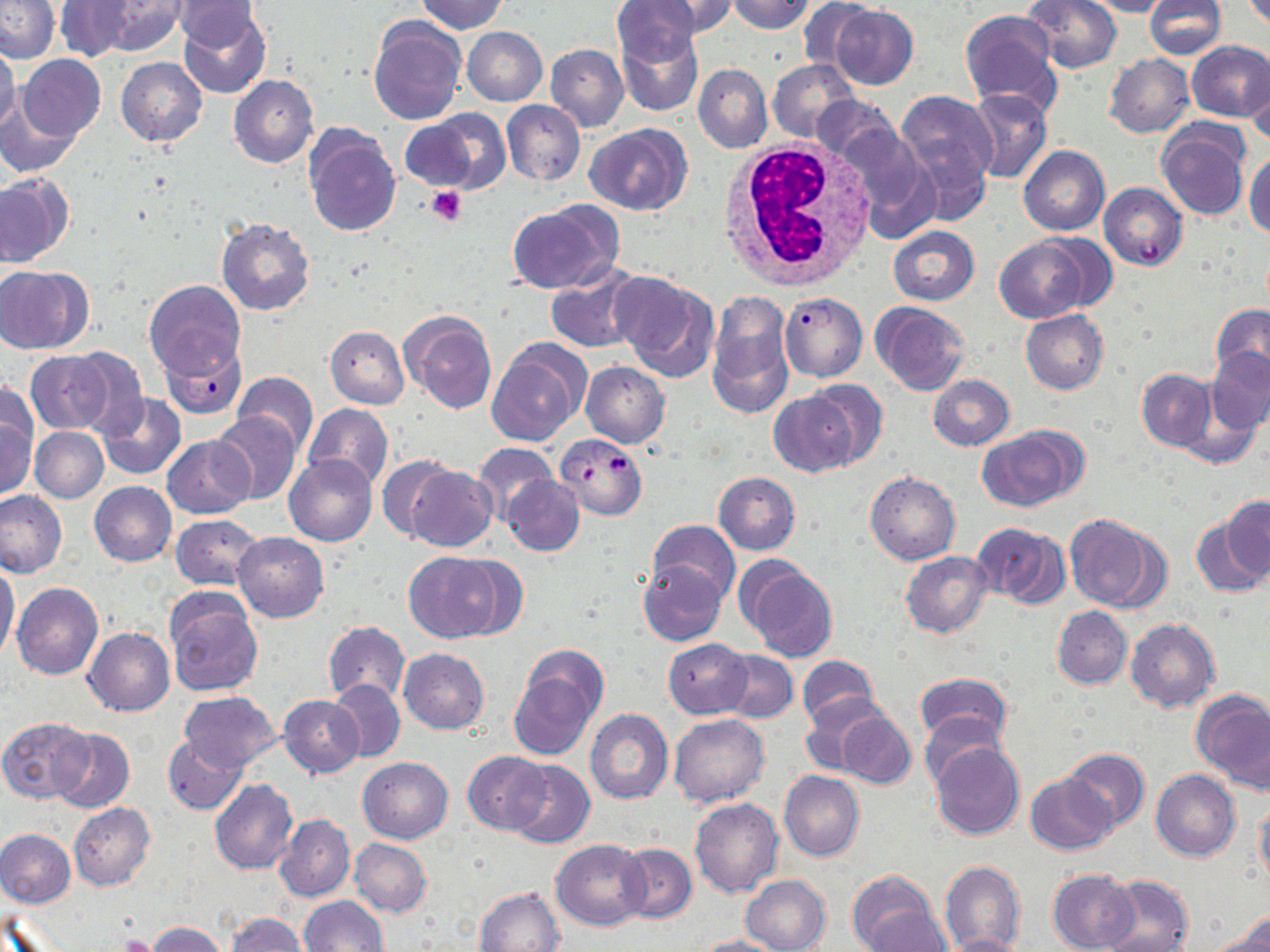
Approximate bounding boxes as named x1/y1/x2/y2 corners in pixels. Plasmodium falciparum-infected red blood cell locations: (x1=1098, y1=183, x2=1188, y2=270), (x1=778, y1=291, x2=867, y2=383), (x1=161, y1=339, x2=246, y2=419), (x1=556, y1=434, x2=648, y2=519). White blood cell locations: (x1=716, y1=139, x2=877, y2=291). Uninfected red blood cell locations: (x1=1, y1=0, x2=60, y2=63), (x1=415, y1=0, x2=508, y2=34), (x1=611, y1=0, x2=707, y2=68), (x1=639, y1=0, x2=743, y2=38), (x1=726, y1=0, x2=817, y2=34), (x1=1024, y1=0, x2=1122, y2=73), (x1=1086, y1=0, x2=1170, y2=18), (x1=1144, y1=0, x2=1227, y2=60), (x1=96, y1=1, x2=187, y2=57), (x1=171, y1=1, x2=265, y2=49), (x1=799, y1=1, x2=873, y2=74), (x1=54, y1=2, x2=133, y2=63), (x1=177, y1=5, x2=271, y2=99), (x1=830, y1=5, x2=918, y2=88), (x1=959, y1=10, x2=1061, y2=112), (x1=369, y1=17, x2=465, y2=125), (x1=616, y1=24, x2=705, y2=118), (x1=463, y1=27, x2=547, y2=106), (x1=1185, y1=40, x2=1270, y2=122), (x1=0, y1=41, x2=20, y2=134), (x1=546, y1=44, x2=629, y2=133), (x1=1104, y1=54, x2=1195, y2=139), (x1=17, y1=55, x2=105, y2=141), (x1=116, y1=57, x2=207, y2=147), (x1=768, y1=59, x2=859, y2=143), (x1=693, y1=64, x2=773, y2=153), (x1=1246, y1=68, x2=1269, y2=145), (x1=228, y1=75, x2=320, y2=169), (x1=965, y1=89, x2=1052, y2=183), (x1=0, y1=90, x2=79, y2=179), (x1=893, y1=93, x2=994, y2=209), (x1=811, y1=94, x2=901, y2=166), (x1=501, y1=99, x2=586, y2=186), (x1=406, y1=111, x2=502, y2=193), (x1=1156, y1=122, x2=1249, y2=221), (x1=586, y1=124, x2=692, y2=216), (x1=304, y1=125, x2=401, y2=237), (x1=832, y1=126, x2=940, y2=244), (x1=1018, y1=146, x2=1109, y2=235), (x1=1245, y1=150, x2=1270, y2=239), (x1=0, y1=173, x2=72, y2=268), (x1=507, y1=203, x2=620, y2=295), (x1=217, y1=218, x2=314, y2=314), (x1=887, y1=225, x2=978, y2=306), (x1=1031, y1=233, x2=1117, y2=312), (x1=994, y1=237, x2=1091, y2=323), (x1=546, y1=261, x2=645, y2=353), (x1=0, y1=265, x2=91, y2=354), (x1=613, y1=274, x2=721, y2=383), (x1=144, y1=279, x2=245, y2=384), (x1=707, y1=291, x2=794, y2=417), (x1=871, y1=302, x2=969, y2=394), (x1=1212, y1=305, x2=1270, y2=386), (x1=400, y1=308, x2=497, y2=415), (x1=1020, y1=310, x2=1109, y2=394), (x1=326, y1=326, x2=409, y2=409), (x1=488, y1=339, x2=591, y2=447), (x1=63, y1=346, x2=149, y2=438), (x1=1206, y1=348, x2=1270, y2=434), (x1=25, y1=351, x2=111, y2=434), (x1=580, y1=361, x2=669, y2=448), (x1=1136, y1=368, x2=1215, y2=451), (x1=232, y1=373, x2=318, y2=455), (x1=928, y1=374, x2=1015, y2=450), (x1=803, y1=379, x2=888, y2=469), (x1=0, y1=380, x2=38, y2=465), (x1=768, y1=391, x2=859, y2=477), (x1=96, y1=392, x2=187, y2=480), (x1=304, y1=404, x2=392, y2=491), (x1=212, y1=412, x2=300, y2=506), (x1=0, y1=419, x2=36, y2=501), (x1=977, y1=426, x2=1084, y2=512), (x1=30, y1=427, x2=109, y2=503), (x1=163, y1=435, x2=254, y2=518), (x1=473, y1=443, x2=559, y2=524), (x1=285, y1=455, x2=376, y2=547), (x1=376, y1=456, x2=458, y2=542), (x1=405, y1=465, x2=497, y2=552), (x1=865, y1=471, x2=960, y2=565), (x1=713, y1=472, x2=801, y2=554), (x1=503, y1=476, x2=584, y2=556), (x1=89, y1=481, x2=177, y2=566), (x1=0, y1=490, x2=69, y2=579), (x1=1224, y1=496, x2=1270, y2=583), (x1=1192, y1=510, x2=1269, y2=598), (x1=172, y1=515, x2=261, y2=590), (x1=1066, y1=516, x2=1162, y2=612), (x1=645, y1=519, x2=740, y2=604), (x1=972, y1=523, x2=1070, y2=609), (x1=234, y1=532, x2=329, y2=622), (x1=403, y1=551, x2=510, y2=642), (x1=900, y1=551, x2=993, y2=639), (x1=638, y1=559, x2=726, y2=646), (x1=739, y1=559, x2=840, y2=663), (x1=0, y1=563, x2=20, y2=661), (x1=12, y1=582, x2=103, y2=680), (x1=163, y1=590, x2=263, y2=698), (x1=1052, y1=606, x2=1132, y2=690), (x1=1125, y1=618, x2=1220, y2=712), (x1=323, y1=622, x2=409, y2=704), (x1=84, y1=628, x2=175, y2=716), (x1=664, y1=638, x2=753, y2=718), (x1=398, y1=648, x2=489, y2=734), (x1=720, y1=650, x2=798, y2=722), (x1=509, y1=654, x2=604, y2=757), (x1=797, y1=655, x2=881, y2=730), (x1=912, y1=673, x2=1013, y2=752), (x1=329, y1=680, x2=406, y2=762), (x1=178, y1=691, x2=281, y2=771), (x1=1193, y1=691, x2=1270, y2=791), (x1=280, y1=694, x2=364, y2=777), (x1=801, y1=694, x2=892, y2=776), (x1=585, y1=709, x2=673, y2=804), (x1=920, y1=709, x2=1006, y2=787), (x1=835, y1=710, x2=915, y2=789), (x1=669, y1=714, x2=769, y2=806), (x1=1, y1=718, x2=95, y2=803), (x1=50, y1=728, x2=135, y2=813), (x1=163, y1=734, x2=248, y2=816), (x1=930, y1=740, x2=1025, y2=840), (x1=1060, y1=748, x2=1150, y2=831), (x1=464, y1=751, x2=551, y2=833), (x1=358, y1=757, x2=453, y2=843), (x1=506, y1=760, x2=594, y2=849), (x1=1151, y1=769, x2=1240, y2=862), (x1=778, y1=771, x2=865, y2=861), (x1=1025, y1=773, x2=1119, y2=855), (x1=210, y1=780, x2=298, y2=875), (x1=691, y1=798, x2=783, y2=897), (x1=1256, y1=798, x2=1270, y2=888), (x1=68, y1=803, x2=156, y2=890), (x1=274, y1=814, x2=355, y2=903), (x1=0, y1=829, x2=76, y2=908), (x1=349, y1=838, x2=432, y2=916), (x1=551, y1=839, x2=650, y2=930), (x1=616, y1=843, x2=696, y2=924), (x1=939, y1=860, x2=1026, y2=951), (x1=846, y1=869, x2=942, y2=952), (x1=1048, y1=870, x2=1141, y2=951), (x1=741, y1=874, x2=832, y2=952), (x1=1100, y1=874, x2=1194, y2=952), (x1=475, y1=887, x2=565, y2=951), (x1=300, y1=896, x2=388, y2=952), (x1=862, y1=906, x2=951, y2=950), (x1=227, y1=913, x2=307, y2=951), (x1=1215, y1=914, x2=1270, y2=952), (x1=149, y1=923, x2=230, y2=952), (x1=939, y1=934, x2=1031, y2=952), (x1=694, y1=936, x2=785, y2=952). Platelet locations: (x1=425, y1=185, x2=467, y2=225), (x1=121, y1=934, x2=157, y2=952). Slide-level diagnosis: Plasmodium falciparum. Thin blood smear. Image is 1270×952 pixels. Single field of view. May-Grünwald-Giemsa stain. Optical microscopy. Captured at 1000x magnification.